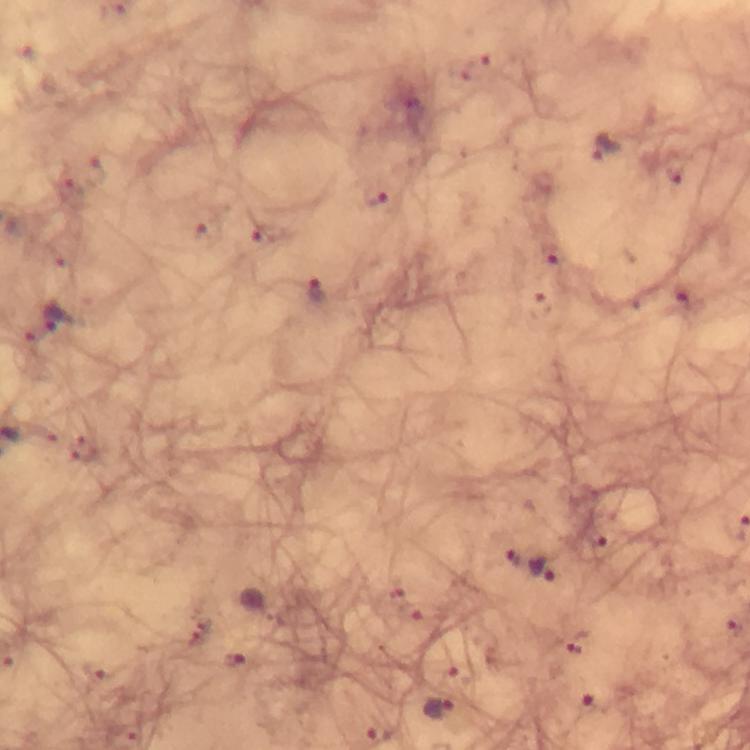

capture: smartphone mounted on the microscope
image_size: 750×750 pixels
preparation: thick blood smear
plasmodium_parasite_locations: 'approximate centers as {x, y} in pixels: {478, 68}, {607, 151}, {376, 197}, {269, 234}, {554, 256}, {317, 291}, {684, 298}, {57, 317}, {514, 555}, {542, 570}, {590, 705}, {439, 711}'
context: from a malaria diagnostic workup
magnification: 100x
stain: Giemsa
cropped_from: one field of view
immersion_oil: applied